State which parasite is depicted.
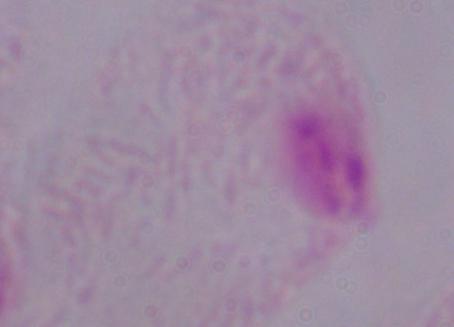

A trichomonad.

magnification: 1000x
modality: photomicrograph